Outline each blood parasite and name the species.
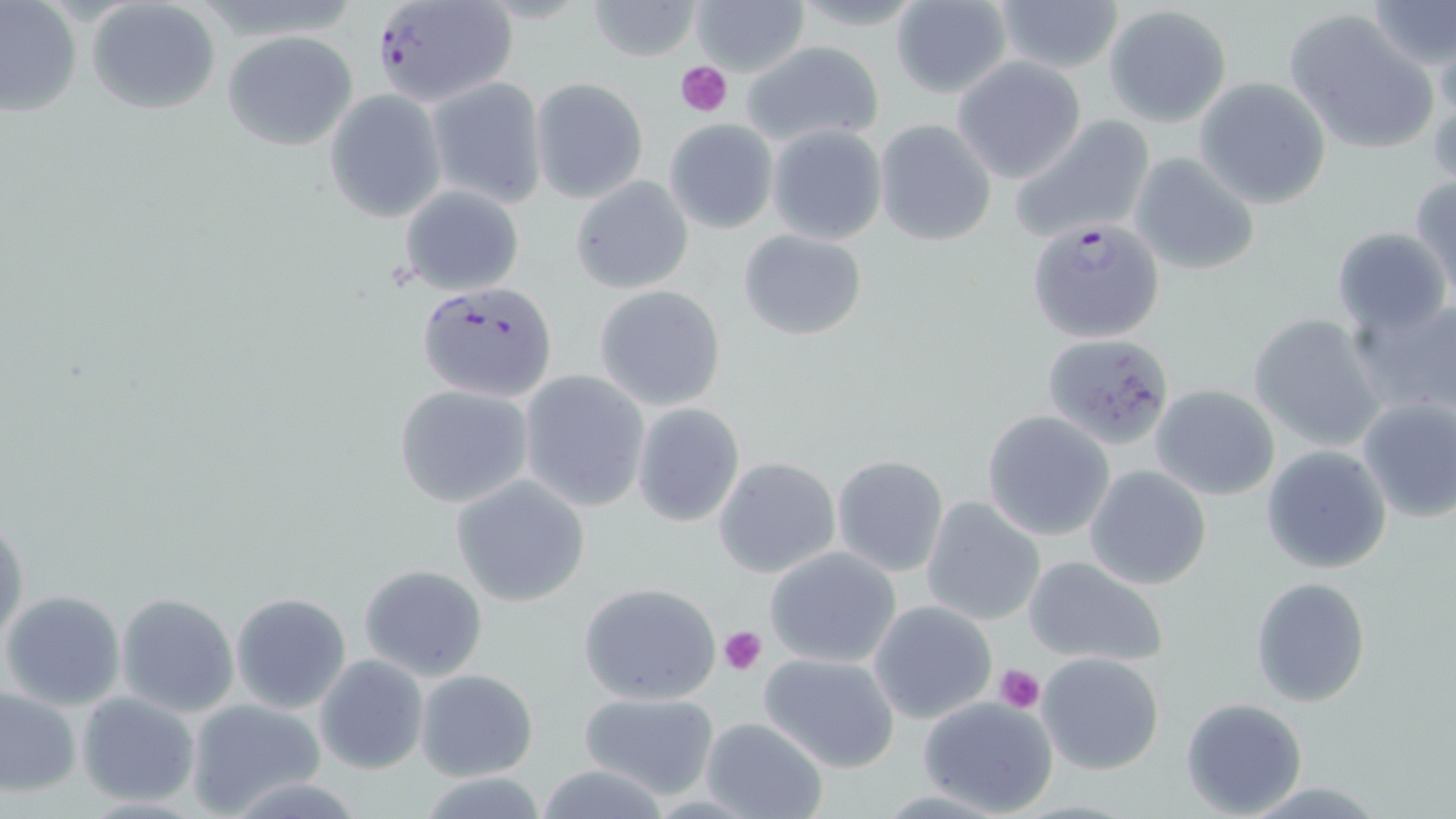
Approximate bounding boxes as (x1,y1)-(x2,y2) corner pairs in pixels.
Plasmodium falciparum-infected red blood cells: (369,0)-(520,109), (1028,217)-(1166,343), (415,280)-(559,404).
No Plasmodium ovale, Plasmodium malariae, Plasmodium vivax, Babesia divergens, or Trypanosoma brucei observed.

Uninfected red blood cell locations: (86,0)-(222,117), (585,0)-(704,61), (990,0)-(1126,75), (1365,0)-(1455,69), (888,1)-(1014,100), (687,2)-(809,75), (0,3)-(80,118), (1104,5)-(1232,127), (1284,7)-(1439,153), (222,31)-(358,151), (741,41)-(885,149), (1428,45)-(1456,174), (952,58)-(1087,185), (425,76)-(548,208), (530,77)-(649,203), (1194,78)-(1331,209), (324,89)-(448,222), (1007,114)-(1155,245), (873,118)-(997,245), (664,119)-(777,234), (766,124)-(887,245), (1126,150)-(1263,278), (572,175)-(694,295), (1409,176)-(1456,296), (397,184)-(525,296), (1330,225)-(1453,337), (738,228)-(867,341), (593,285)-(728,411), (1349,294)-(1456,419), (1248,313)-(1385,452), (1037,331)-(1169,446), (516,369)-(650,512), (393,382)-(534,508), (1149,384)-(1280,500), (1353,394)-(1456,525), (630,403)-(745,527), (981,410)-(1115,540), (1262,443)-(1392,574), (830,455)-(948,577), (713,457)-(841,578), (1085,465)-(1213,590), (451,475)-(591,607), (920,496)-(1047,626), (0,511)-(27,648), (763,547)-(902,669), (1022,554)-(1170,669), (356,564)-(489,681), (1249,577)-(1372,706), (577,581)-(721,707), (1,589)-(127,710), (230,592)-(352,715), (115,593)-(239,717), (868,601)-(997,724), (758,651)-(900,772), (1036,652)-(1165,775), (313,654)-(429,775), (415,668)-(539,781), (0,685)-(81,797), (76,691)-(199,806), (576,691)-(721,801), (183,697)-(327,815), (918,697)-(1058,816), (1180,697)-(1308,817), (699,716)-(830,819), (418,774)-(552,817). Platelet locations: (675,58)-(733,117), (718,625)-(767,674), (994,665)-(1046,714). Slide-level diagnosis: Plasmodium falciparum. May-Grünwald-Giemsa stain. Optical microscopy. Thin blood film. One field of a larger specimen. 1000x magnification. Image is 1456×819 pixels.